Mark where cells are.
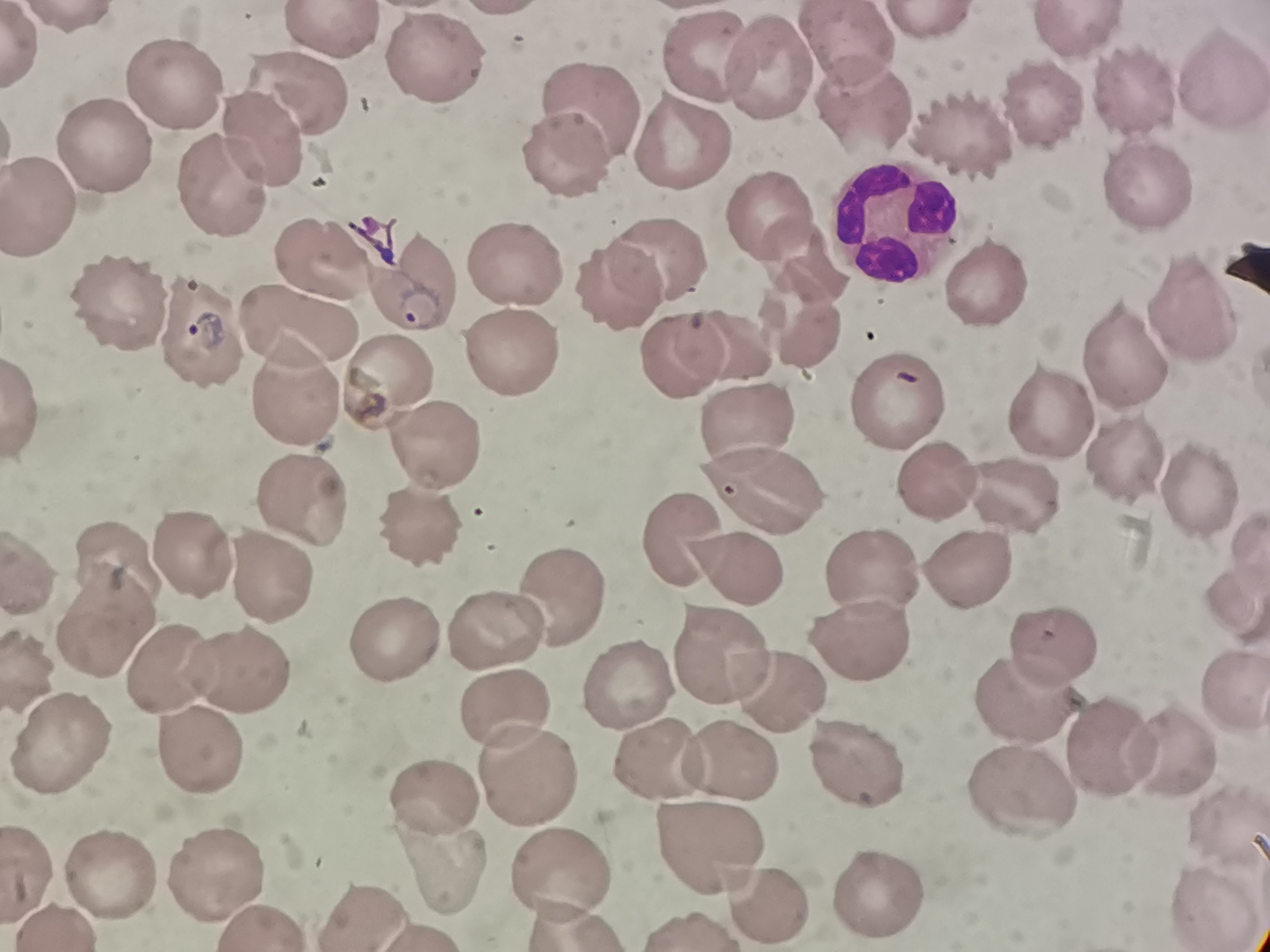

Approximate centers as [x, y] in pixels.
Cells: [927, 24], [1076, 32], [333, 34], [850, 52], [701, 58], [439, 62], [764, 70], [1213, 75], [173, 83], [1131, 89], [290, 91], [860, 103], [1038, 103], [590, 108], [961, 125], [251, 140], [684, 140], [97, 142], [561, 153], [1141, 184], [222, 186], [41, 211], [763, 216], [895, 221], [320, 255], [658, 256], [802, 258], [513, 263], [980, 278], [411, 279], [624, 286], [119, 299], [1195, 307], [299, 321], [206, 329], [819, 334], [733, 339], [512, 354], [686, 356], [1125, 360], [391, 377], [296, 388], [896, 393], [1048, 410], [743, 421], [434, 446], [1125, 451], [936, 478], [762, 488], [1187, 488], [1012, 491], [301, 496], [416, 525], [1243, 540], [195, 551], [971, 561], [119, 562], [879, 568], [270, 573], [568, 600], [1232, 600], [108, 625], [501, 627], [860, 632], [394, 640], [1054, 644], [729, 654], [170, 670], [240, 670], [626, 680], [779, 683], [1234, 684], [1015, 696], [508, 702], [1109, 744], [1173, 744], [63, 746], [198, 751], [861, 758], [737, 759], [660, 762], [529, 769], [1026, 786], [435, 793], [1226, 817], [701, 847], [436, 860], [558, 871], [108, 872], [217, 874], [879, 891], [772, 898], [1214, 904], [361, 911].

Summary:
  - Preparation: thin smear
  - Image size: 1270×952 pixels
  - Field of view: single
  - Capture: smartphone camera at the microscope eyepiece
  - Stain: Giemsa